Name the parasite shown.
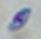

Toxoplasma gondii.

modality = micrograph
magnification = 1000x